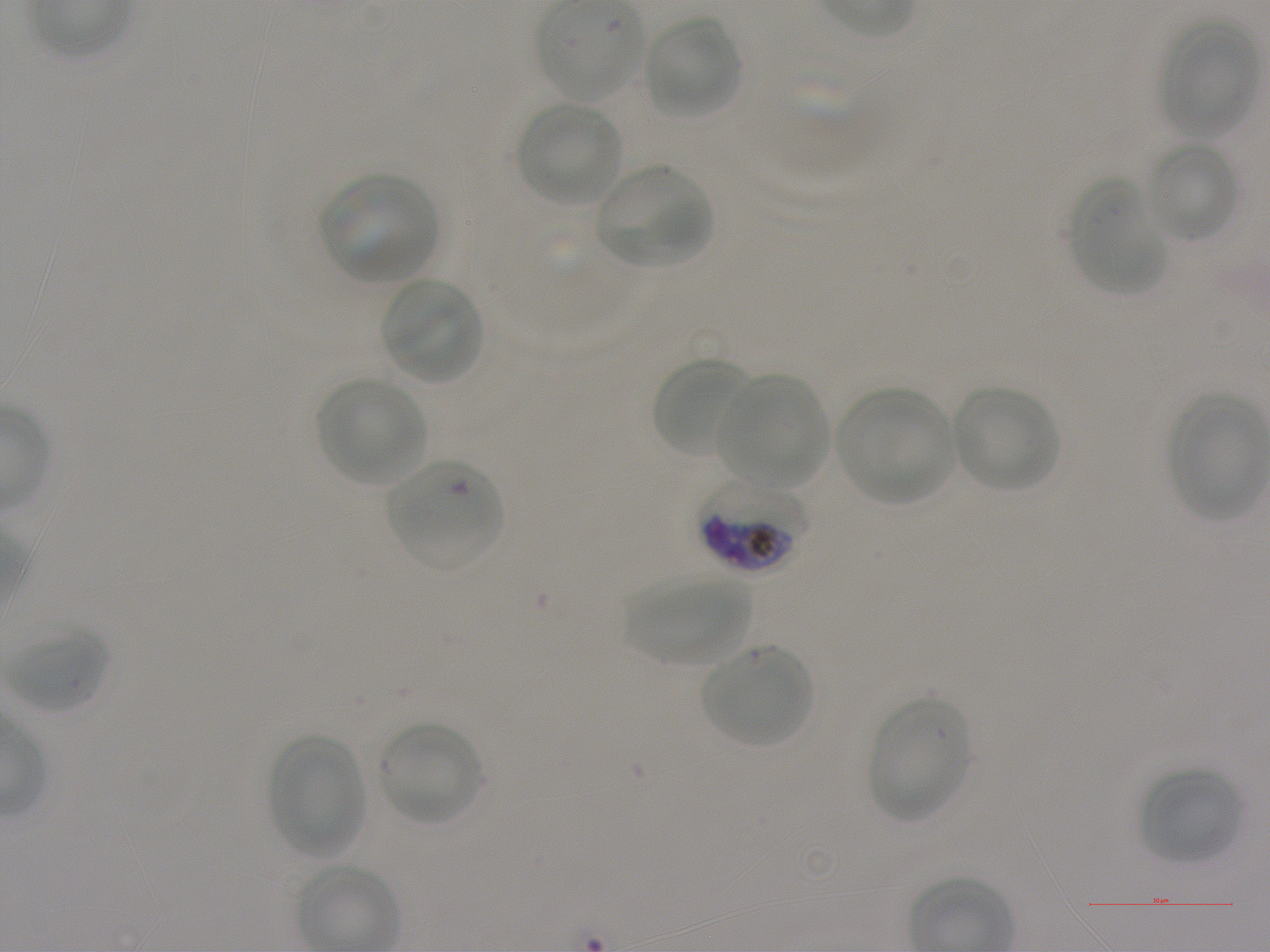

Not every red blood cell is marked. A life-cycle stage — or a range of stages, where the recorded stages span more than one — follows each staged infected red blood cell.
{
  "stain": "Giemsa",
  "locations_of_infected_red_blood_cells": "approximate bounding rectangles given as corner coordinates in pixels from the top-left: (x1=699, y1=479, x2=810, y2=574) late trophozoite to early schizont",
  "donor_blood_group": "A+",
  "locations_of_uninfected_red_blood_cells": "approximate bounding rectangles given as corner coordinates in pixels from the top-left: (x1=537, y1=4, x2=646, y2=103), (x1=643, y1=15, x2=741, y2=119), (x1=1159, y1=20, x2=1259, y2=138), (x1=517, y1=102, x2=622, y2=206), (x1=1145, y1=140, x2=1240, y2=243), (x1=594, y1=165, x2=712, y2=269), (x1=319, y1=174, x2=439, y2=283), (x1=1070, y1=182, x2=1168, y2=296), (x1=380, y1=278, x2=483, y2=385), (x1=650, y1=356, x2=753, y2=460), (x1=718, y1=374, x2=828, y2=490), (x1=317, y1=377, x2=426, y2=485), (x1=951, y1=385, x2=1060, y2=492), (x1=836, y1=389, x2=957, y2=505), (x1=1169, y1=395, x2=1267, y2=519), (x1=625, y1=575, x2=752, y2=667), (x1=6, y1=624, x2=108, y2=713), (x1=699, y1=643, x2=815, y2=749), (x1=868, y1=698, x2=970, y2=822), (x1=378, y1=720, x2=483, y2=826), (x1=269, y1=735, x2=367, y2=857), (x1=1139, y1=767, x2=1244, y2=865)",
  "locations_of_red_blood_cells_of_indeterminate_infection_status": "approximate bounding rectangles given as corner coordinates in pixels from the top-left: (x1=386, y1=460, x2=504, y2=570)",
  "objective": "100x, oil immersion, numerical aperture 1.25",
  "culture": "static in-vitro Plasmodium falciparum strain NF54",
  "field_of_view": "single",
  "preparation": "thin blood smear",
  "image_size": "1270×952 pixels"
}